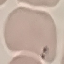

{
  "result": "malaria parasites identified",
  "preparation": "thin blood film",
  "image_type": "automatically extracted cell patch, resized to 64 × 64 pixels",
  "capture": "smartphone through the microscope eyepiece",
  "stain": "Giemsa"
}